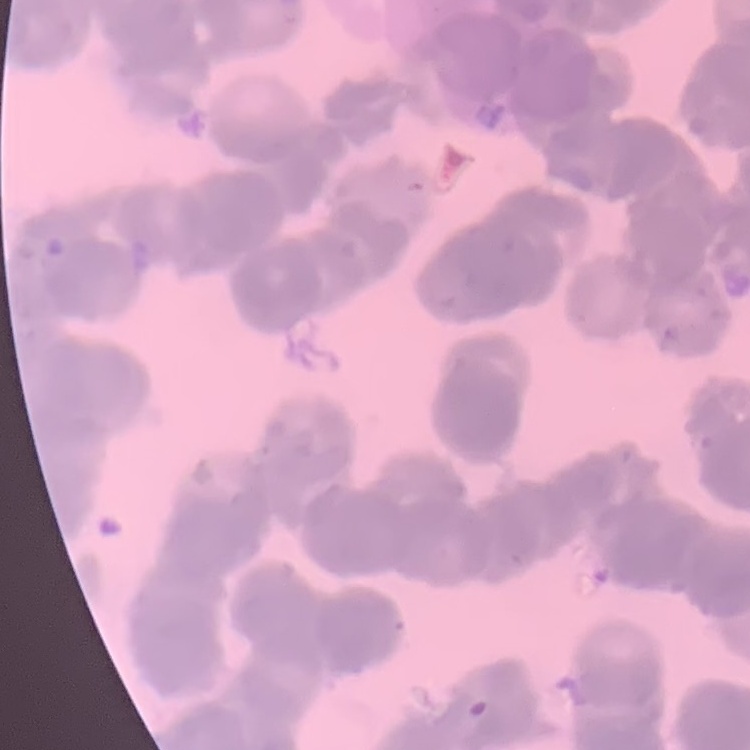
Summary:
  - Red blood cell morphology: rouleaux formation
  - Preparation: thin blood film
  - Image type: square crop of a larger photomicrograph
  - Stain: Field's or Giemsa